Point out each Plasmodium parasite.
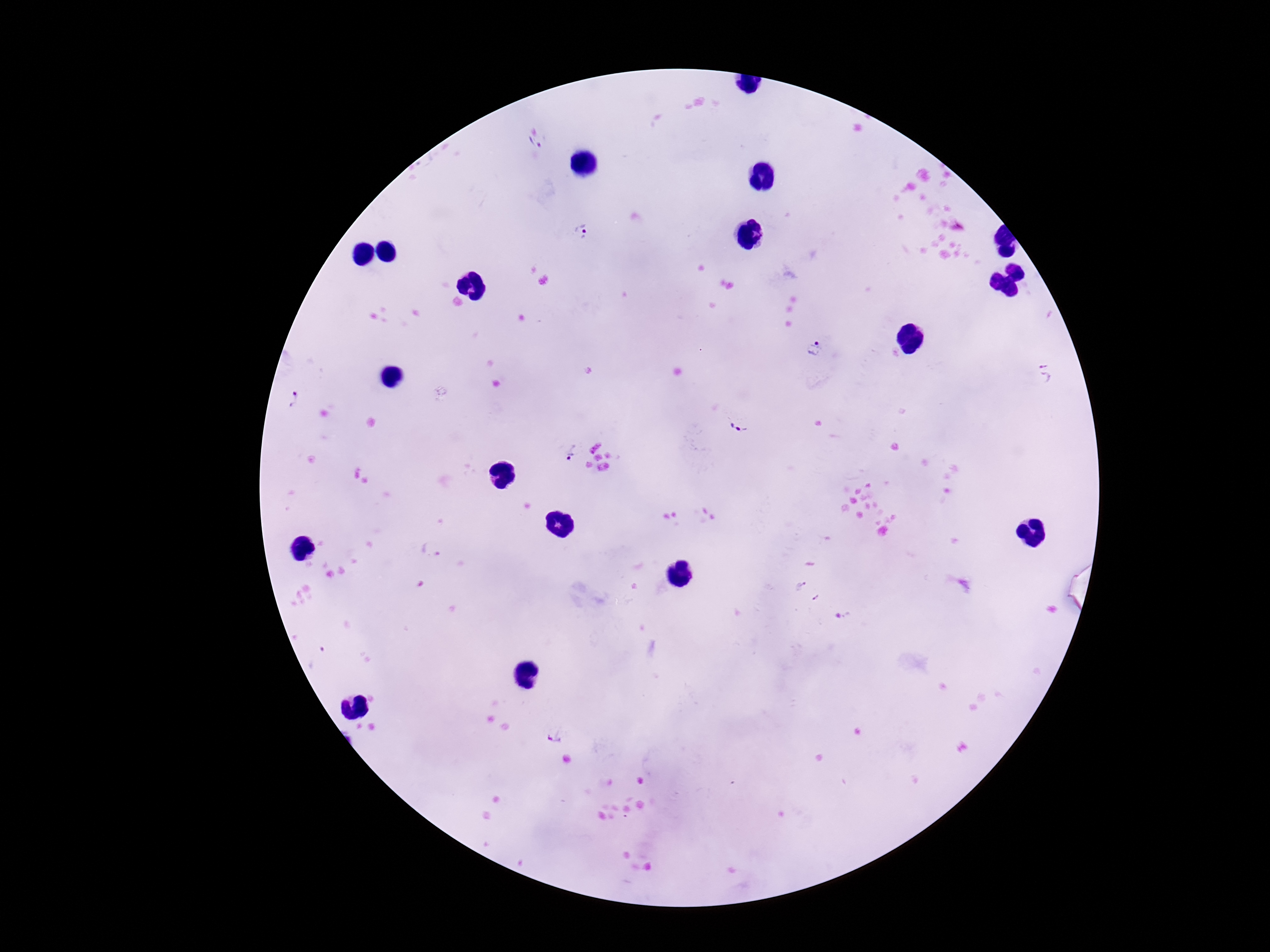
Approximate centers as [x, y] in pixels.
Plasmodium parasites: [539, 144], [579, 231], [815, 347], [1046, 371], [294, 400], [740, 425], [571, 450], [432, 549], [800, 586], [815, 599], [555, 735].

Summary:
  - Patient malaria status: positive
  - Magnification: 100x
  - Image size: 1270×952 pixels
  - Capture: smartphone camera through the microscope eyepiece
  - Preparation: thick peripheral-blood smear
  - Field of view: single
  - Stain: Giemsa